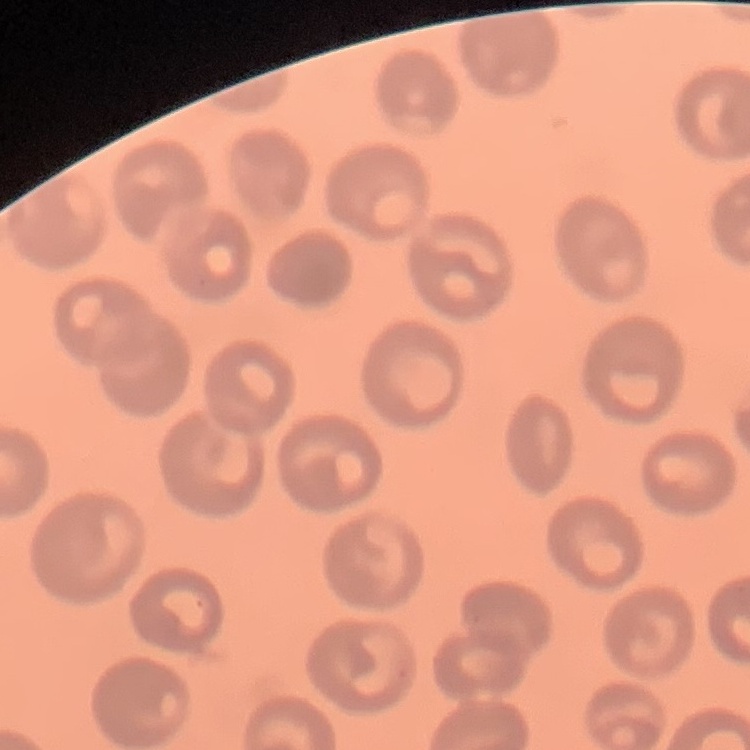

{
  "erythrocyte_morphology": "no rouleaux formation",
  "stain": "Field's or Giemsa",
  "image_type": "one tile cut from a larger photomicrograph",
  "preparation": "thin blood film"
}